State which cell type is depicted.
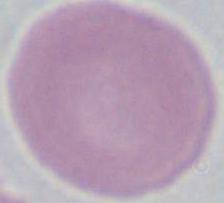
An erythrocyte.

modality = photomicrograph
magnification = 1000x